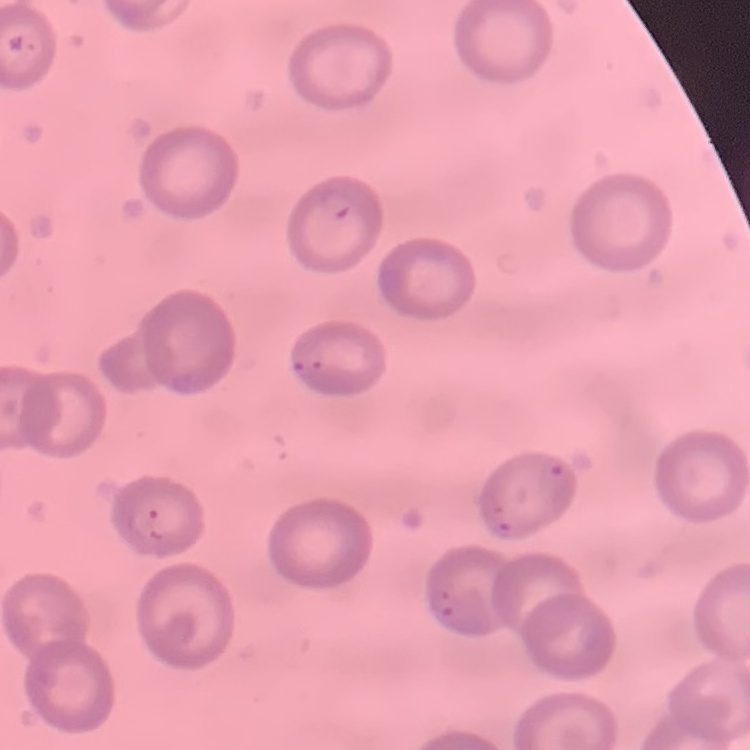
The red blood cells show no rouleaux formation. Square crop of a larger photomicrograph. Thin blood smear. Stained with either Field's or Giemsa.